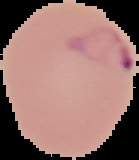

Summary:
  - Image size: 139×160 pixels
  - Result: Plasmodium parasites detected
  - Image type: cell region segmented out of the field of view; surrounding area masked to black
  - Preparation: thin blood film